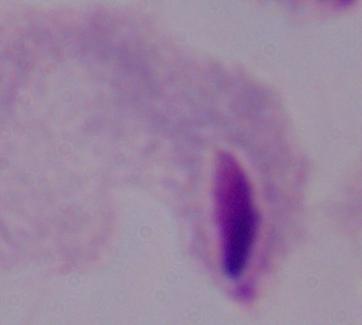

Photomicrograph. A trichomonad is shown. 1000x magnification.